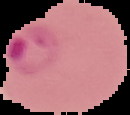

Image is 130×115 pixels. Result: malaria parasites identified. From a thin blood film. Segmented cell region on a black background.